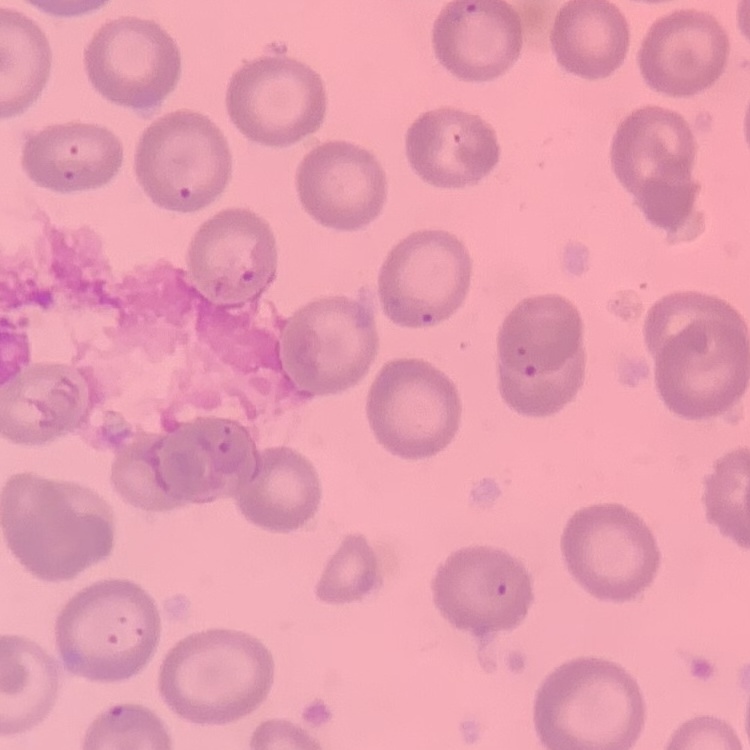
erythrocyte morphology = no rouleaux formation
preparation = thin blood film
stain = Field's or Giemsa
image type = one tile cut from a larger photomicrograph